Mark where platelets are.
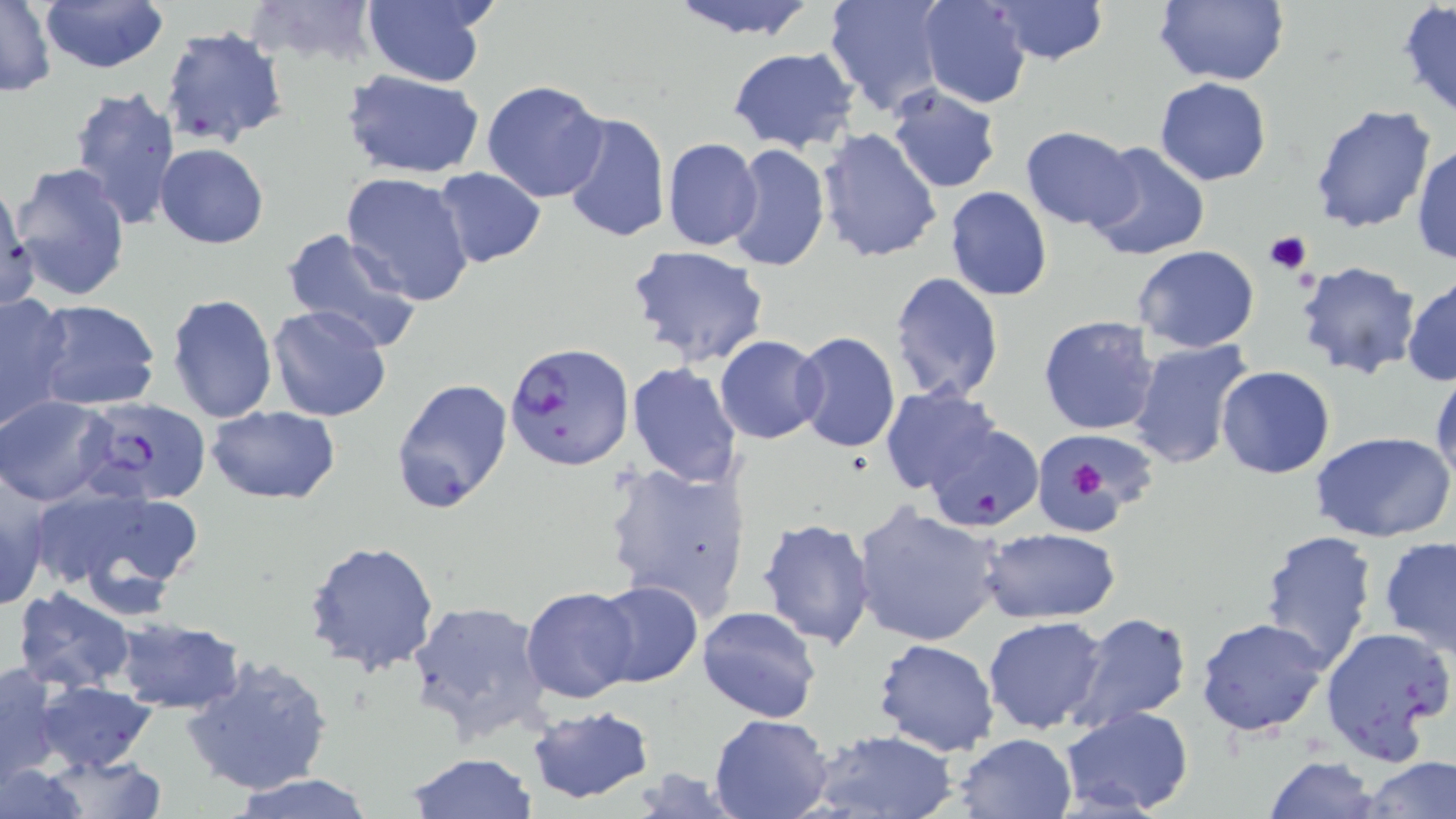
Approximate bounding boxes as (x1,y1)-(x2,y2) corner pairs in pixels.
Platelets: (1263,230)-(1312,275), (1071,464)-(1109,497).

Summary:
  - Uninfected red blood cell locations: (37,0)-(169,72), (245,0)-(383,68), (361,0)-(490,87), (665,0)-(824,40), (822,0)-(945,116), (917,0)-(1032,108), (989,0)-(1110,64), (1152,0)-(1290,87), (1,1)-(56,97), (1398,2)-(1456,122), (159,26)-(289,148), (727,46)-(860,154), (343,70)-(484,179), (1154,78)-(1272,185), (482,79)-(609,202), (68,84)-(182,228), (886,84)-(1003,194), (1309,103)-(1440,234), (558,109)-(671,244), (1019,126)-(1142,231), (818,128)-(943,264), (662,137)-(763,251), (1085,140)-(1213,261), (155,143)-(269,248), (726,143)-(831,273), (1412,144)-(1456,265), (8,163)-(130,302), (433,166)-(547,267), (340,171)-(475,306), (944,185)-(1054,302), (0,187)-(37,312), (279,229)-(426,353), (625,245)-(772,368), (1131,246)-(1260,352), (1295,260)-(1423,381), (890,271)-(1005,403), (1403,273)-(1456,387), (0,292)-(75,429), (167,292)-(278,424), (32,300)-(161,412), (266,304)-(393,423), (1037,315)-(1161,437), (791,331)-(900,453), (715,336)-(826,443), (1128,338)-(1259,472), (625,361)-(743,486), (1430,363)-(1456,488), (1215,367)-(1336,479), (390,377)-(514,514), (880,388)-(1002,496), (0,395)-(114,505), (208,405)-(340,503), (924,423)-(1043,533), (1311,431)-(1456,543), (1038,433)-(1166,536), (603,458)-(753,621), (30,482)-(208,612), (0,483)-(52,612), (853,503)-(1004,647), (756,518)-(874,651), (979,527)-(1121,624), (1258,529)-(1379,671), (302,537)-(441,674), (1379,537)-(1456,657), (592,580)-(703,686), (521,585)-(640,705), (13,587)-(137,695), (406,600)-(551,741), (696,604)-(821,726), (1067,610)-(1193,734), (983,616)-(1109,735), (1196,616)-(1327,737), (115,617)-(245,713), (1321,625)-(1455,765), (872,637)-(1001,756), (182,652)-(333,797), (1,661)-(65,783), (33,680)-(157,774), (525,704)-(657,803), (1059,706)-(1195,818), (708,711)-(834,819), (810,727)-(961,819), (952,732)-(1077,818), (37,753)-(168,819), (403,753)-(538,819), (1364,755)-(1455,818), (1264,757)-(1381,818), (0,760)-(87,817), (228,772)-(381,819)
  - Plasmodium falciparum-infected red blood cell locations: (505,341)-(634,472), (79,396)-(210,505)
  - Slide-level diagnosis: Plasmodium falciparum
  - Preparation: thin blood film
  - Image size: 1456×819 pixels
  - Field of view: single
  - Modality: light microscopy
  - Magnification: 1000x
  - Stain: May-Grünwald-Giemsa